Classify this cell by malaria status.
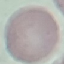
It is uninfected.

Thin smear of blood. Automatically extracted cell patch, resized to 64 × 64 pixels. Giemsa stain. Photographed with a smartphone camera at the microscope eyepiece.